Comment on the morphology of the red blood cells.
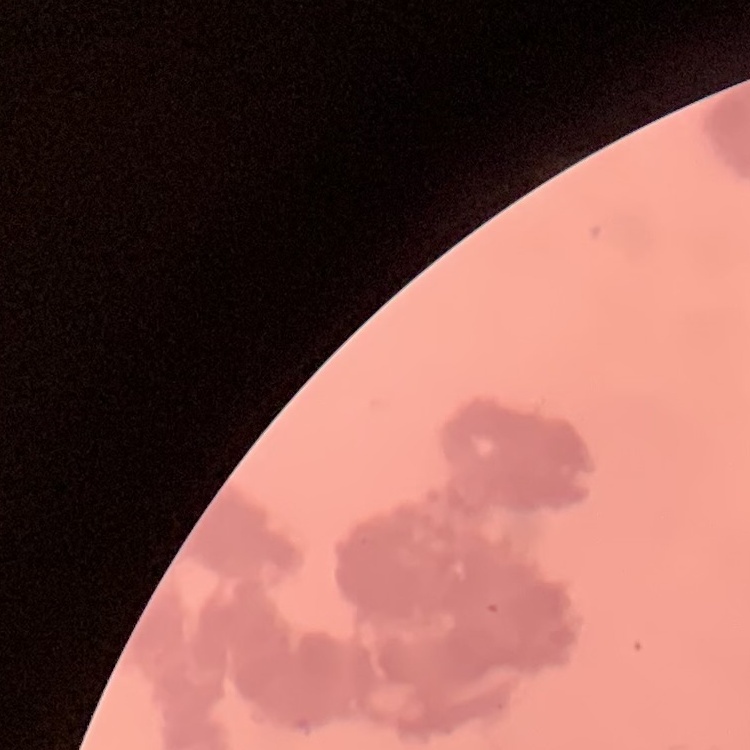
Rouleaux formation.

image type = square crop of a larger photomicrograph
stain = Field's or Giemsa
preparation = thin peripheral smear